Outline platelets.
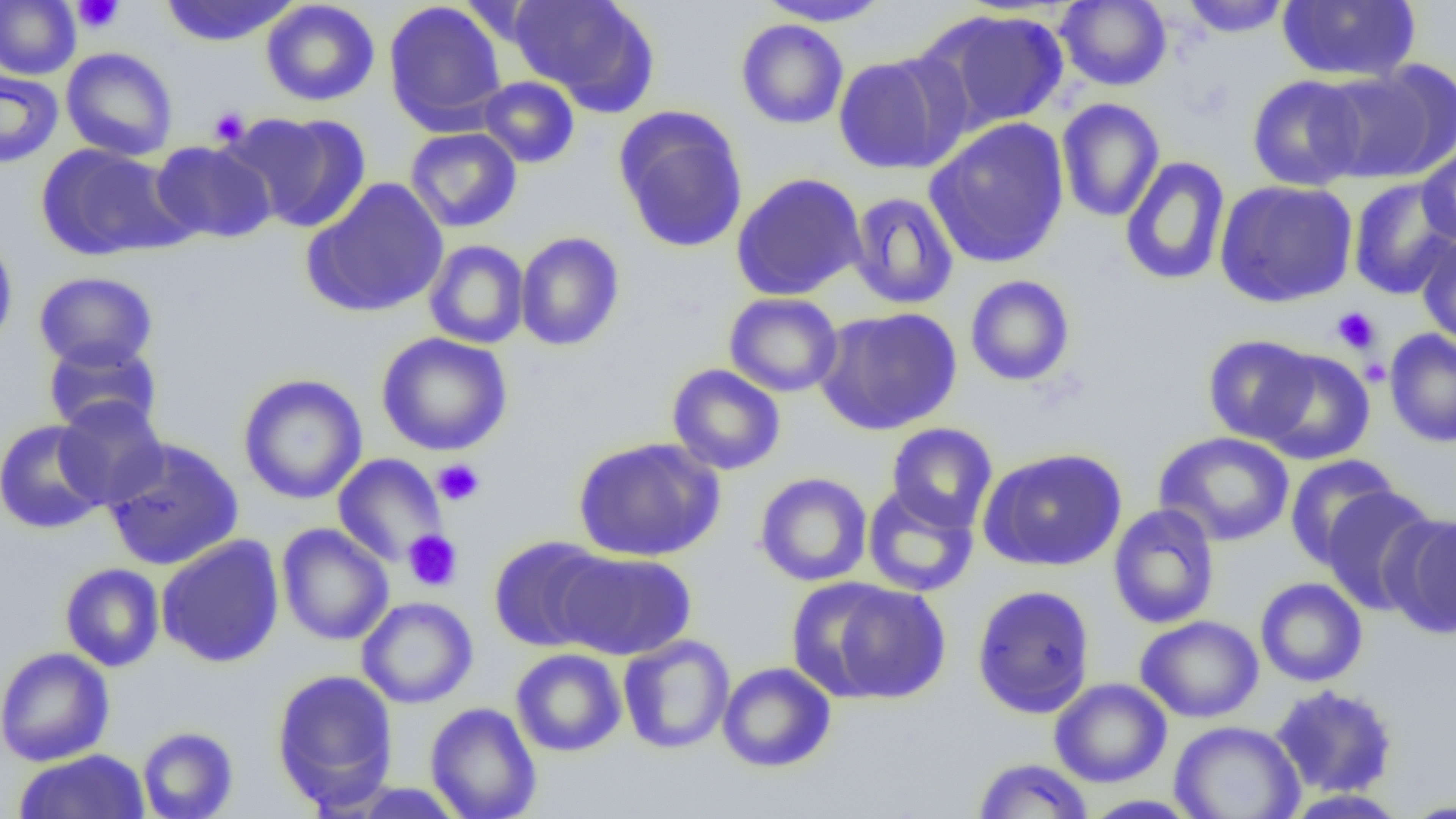
Approximate bounding boxes as (x1, y1, x2, y2) in pixels.
Platelets: (73, 0, 122, 33), (209, 107, 250, 146), (1331, 306, 1380, 354), (1361, 357, 1391, 387), (432, 458, 485, 506), (403, 530, 463, 592).

slide-level diagnosis = negative for blood parasites
preparation = thin blood smear
uninfected red blood cell locations = approximate bounding boxes as (x1, y1, x2, y2) in pixels: (0, 0, 80, 79), (159, 0, 298, 47), (260, 0, 380, 107), (509, 0, 659, 114), (755, 0, 894, 26), (1181, 0, 1292, 38), (383, 1, 507, 134), (1056, 1, 1172, 91), (1277, 1, 1421, 83), (915, 8, 1069, 134), (735, 19, 849, 129), (60, 47, 178, 161), (832, 53, 966, 175), (1318, 61, 1456, 184), (0, 68, 63, 169), (1247, 75, 1367, 191), (478, 76, 580, 168), (1056, 98, 1165, 223), (614, 107, 749, 254), (223, 111, 372, 235), (924, 117, 1070, 269), (405, 127, 522, 233), (150, 139, 277, 244), (1416, 142, 1456, 246), (35, 143, 191, 262), (1119, 155, 1232, 287), (730, 173, 867, 301), (300, 177, 450, 318), (1347, 177, 1456, 300), (1214, 179, 1358, 308), (847, 192, 959, 310), (0, 231, 19, 357), (514, 231, 625, 352), (1416, 233, 1456, 349), (424, 240, 529, 349), (33, 271, 159, 372), (964, 274, 1075, 387), (723, 292, 844, 398), (814, 306, 962, 435), (1384, 329, 1456, 448), (376, 332, 513, 456), (1203, 334, 1320, 445), (42, 338, 163, 436), (1256, 349, 1376, 465), (667, 364, 785, 475), (237, 373, 368, 505), (53, 397, 168, 509), (0, 419, 109, 535), (886, 422, 998, 532), (1154, 431, 1295, 547), (573, 436, 725, 562), (102, 438, 244, 571), (978, 447, 1127, 572), (332, 453, 447, 567), (1284, 454, 1403, 569), (754, 472, 873, 587), (862, 484, 979, 597), (1320, 485, 1439, 616), (1107, 504, 1220, 629), (1385, 513, 1455, 638), (276, 523, 394, 646), (156, 535, 285, 668), (488, 536, 613, 652), (554, 550, 697, 660), (59, 563, 165, 672), (1254, 577, 1368, 687), (805, 579, 951, 704), (971, 584, 1096, 718), (356, 596, 479, 709), (1135, 615, 1264, 723), (618, 634, 735, 754), (0, 647, 114, 766), (510, 648, 626, 757), (717, 661, 837, 773), (271, 668, 399, 812), (1049, 677, 1172, 788), (1268, 684, 1399, 799), (424, 702, 541, 819), (1169, 720, 1306, 819), (137, 726, 238, 818), (13, 749, 150, 819), (972, 758, 1095, 818), (1279, 788, 1413, 818), (1078, 794, 1204, 818), (1396, 796, 1456, 817)
modality = optical microscopy
field of view = one of a larger specimen
image size = 1456×819 pixels
magnification = 1000x